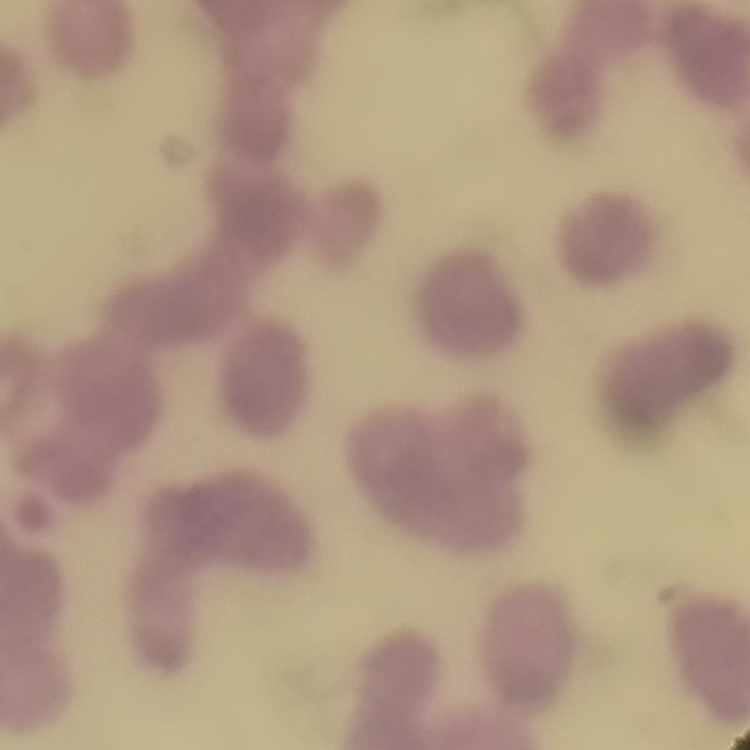

{
  "erythrocyte_morphology": "rouleaux formation",
  "image_type": "one tile cut from a larger photomicrograph",
  "preparation": "thin blood film",
  "stain": "Field's or Giemsa"
}